Assess for malaria.
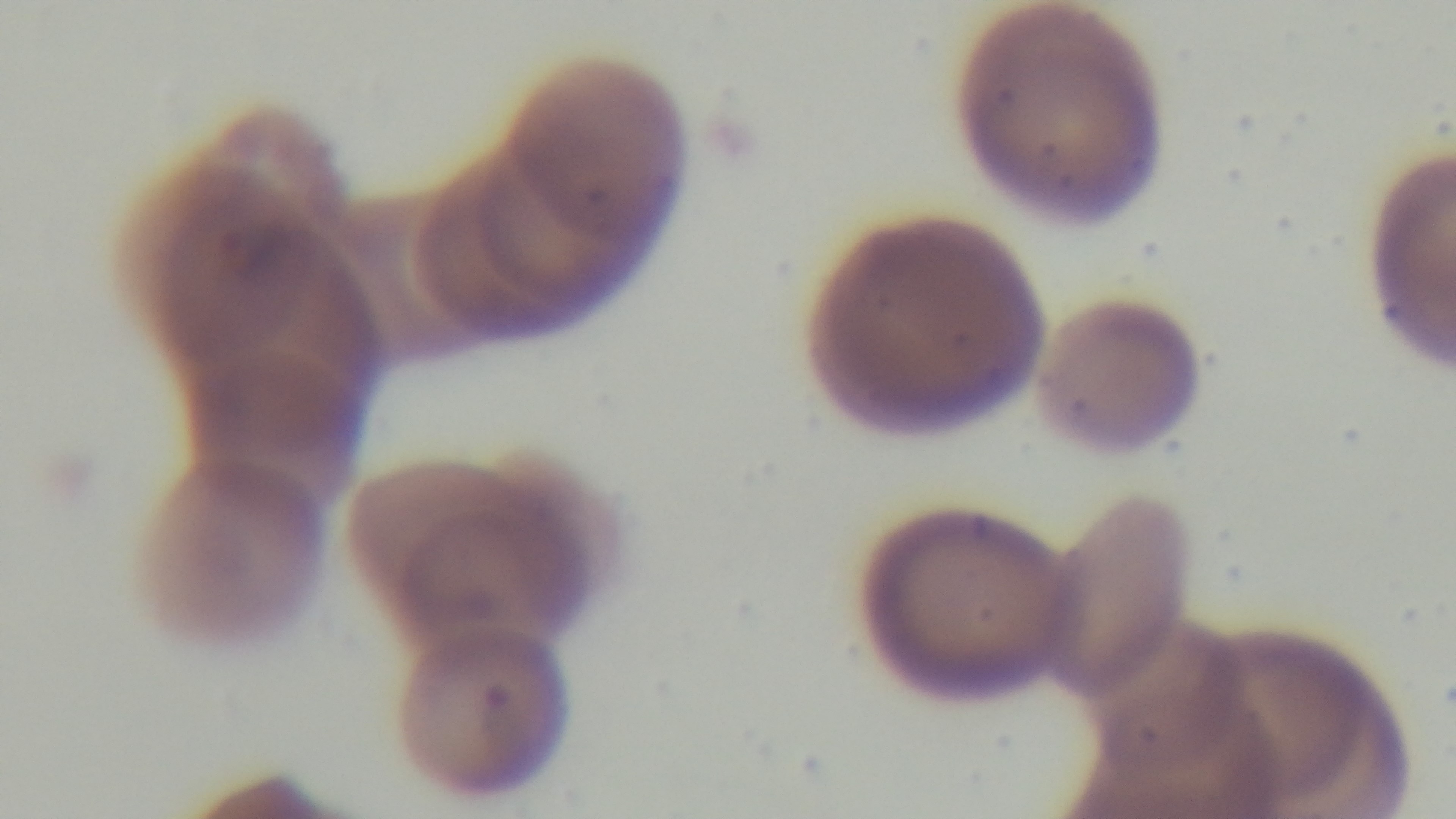

Positive.

Summary:
  - Modality: light microscopy
  - Capture: mounted 4K digital camera
  - Preparation: thin smear
  - Field of view: single
  - Objective: 100x oil immersion
  - Stain: Giemsa